Locate the cells, classifying each as a parasitized red blood cell, an uninfected red blood cell, or a white blood cell.
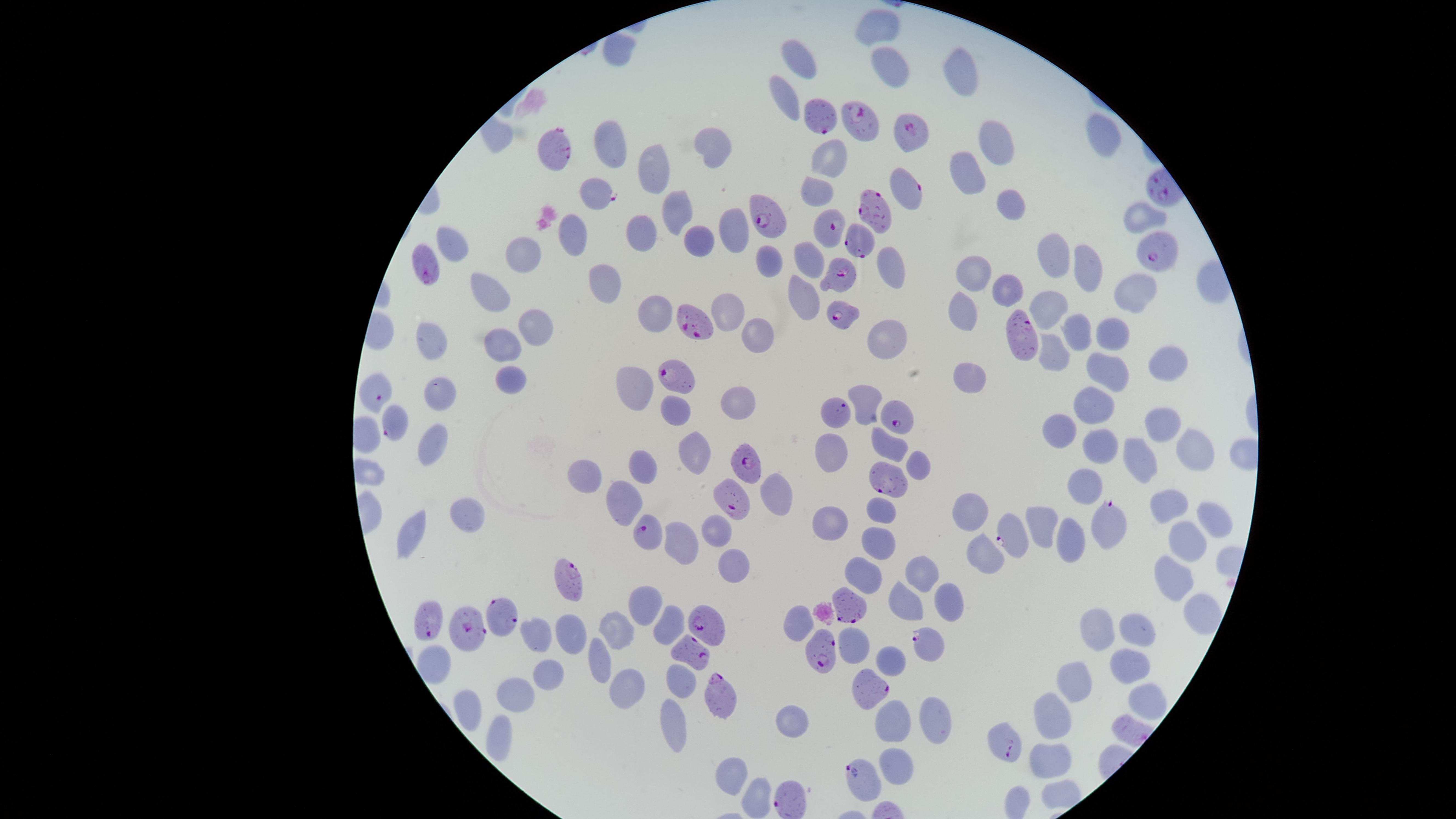

Approximate marker points as (x, y) in pixels.
Parasitized red blood cells: (823, 115), (858, 120), (910, 133), (560, 154), (907, 190), (598, 195), (878, 215), (768, 218), (830, 228), (863, 241), (1147, 252), (426, 269), (839, 277), (839, 314), (693, 326), (1026, 341), (676, 379), (371, 390), (838, 415), (898, 420), (392, 424), (750, 460), (892, 477), (734, 497), (1106, 524), (1012, 535), (653, 536), (575, 583), (852, 610), (500, 615), (432, 622), (706, 627), (471, 632), (935, 639), (691, 649), (824, 651), (869, 686), (724, 698), (1004, 742), (859, 782), (791, 803).
Uninfected red blood cells: (881, 27), (617, 48), (801, 59), (891, 68), (960, 77), (786, 92), (1103, 135), (999, 138), (607, 140), (711, 145), (828, 154), (650, 169), (965, 172), (817, 194), (1010, 202), (674, 209), (1137, 219), (728, 225), (642, 230), (577, 235), (694, 242), (453, 245), (522, 255), (1053, 256), (761, 258), (811, 261), (1078, 267), (891, 268), (974, 276), (605, 283), (491, 287), (1134, 289), (801, 292), (1014, 292), (1046, 305), (728, 308), (653, 314), (965, 314), (534, 325), (1078, 325), (753, 329), (1112, 331), (888, 338), (435, 341), (503, 344), (1057, 358), (1158, 368), (1112, 375), (963, 377), (512, 378), (628, 379), (436, 391), (735, 395), (866, 400), (1093, 404), (678, 408), (1164, 424), (1060, 431), (427, 444), (1095, 444), (890, 445), (696, 448), (827, 448), (1192, 449), (1139, 458), (640, 462), (915, 463), (592, 473), (1077, 484), (775, 494), (624, 500), (1168, 503), (973, 513), (882, 514), (470, 515), (1043, 517), (1211, 518), (829, 525), (716, 530), (412, 532), (1191, 536), (1067, 538), (877, 542), (685, 544), (980, 559), (734, 563), (867, 569), (927, 572), (1175, 578), (908, 597), (951, 600), (646, 608), (1189, 611), (799, 620), (674, 624), (1102, 629), (1138, 629), (616, 631), (571, 635), (536, 637), (856, 641), (893, 656), (593, 662), (434, 663), (1133, 667), (545, 673), (1080, 682), (676, 684), (624, 685), (514, 692), (1144, 699), (465, 706), (935, 714), (1051, 716), (668, 722), (795, 722), (893, 723), (496, 734), (1048, 762), (900, 765), (732, 771), (752, 793).
No white blood cells identified.

Summary:
  - Species: Plasmodium falciparum
  - Field of view: single
  - Preparation: thin blood film
  - Capture: smartphone photograph through the microscope eyepiece
  - Image size: 1456×819 pixels
  - Visible region: circular
  - Stain: Giemsa